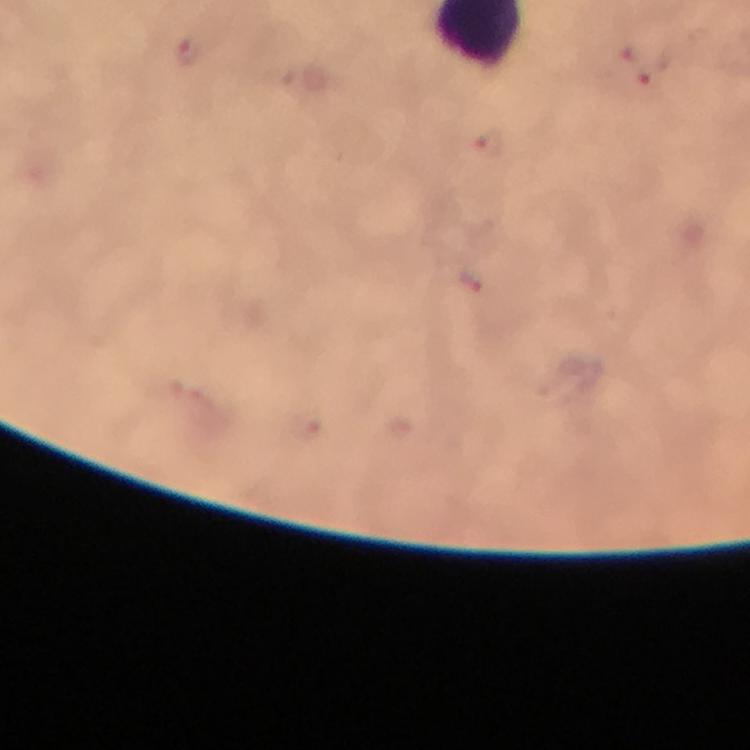

Approximate centers as {x, y} in pixels. Malaria parasite locations: {188, 51}, {638, 66}, {489, 149}, {470, 282}. Photographed with a smartphone mounted on the microscope. From a diagnostic examination for malaria. Giemsa-stained preparation. Image is 750×750 pixels. Immersion oil was used. Thick blood film. 100x magnification. Cropped region of a single field of view.